Comment on the background quality.
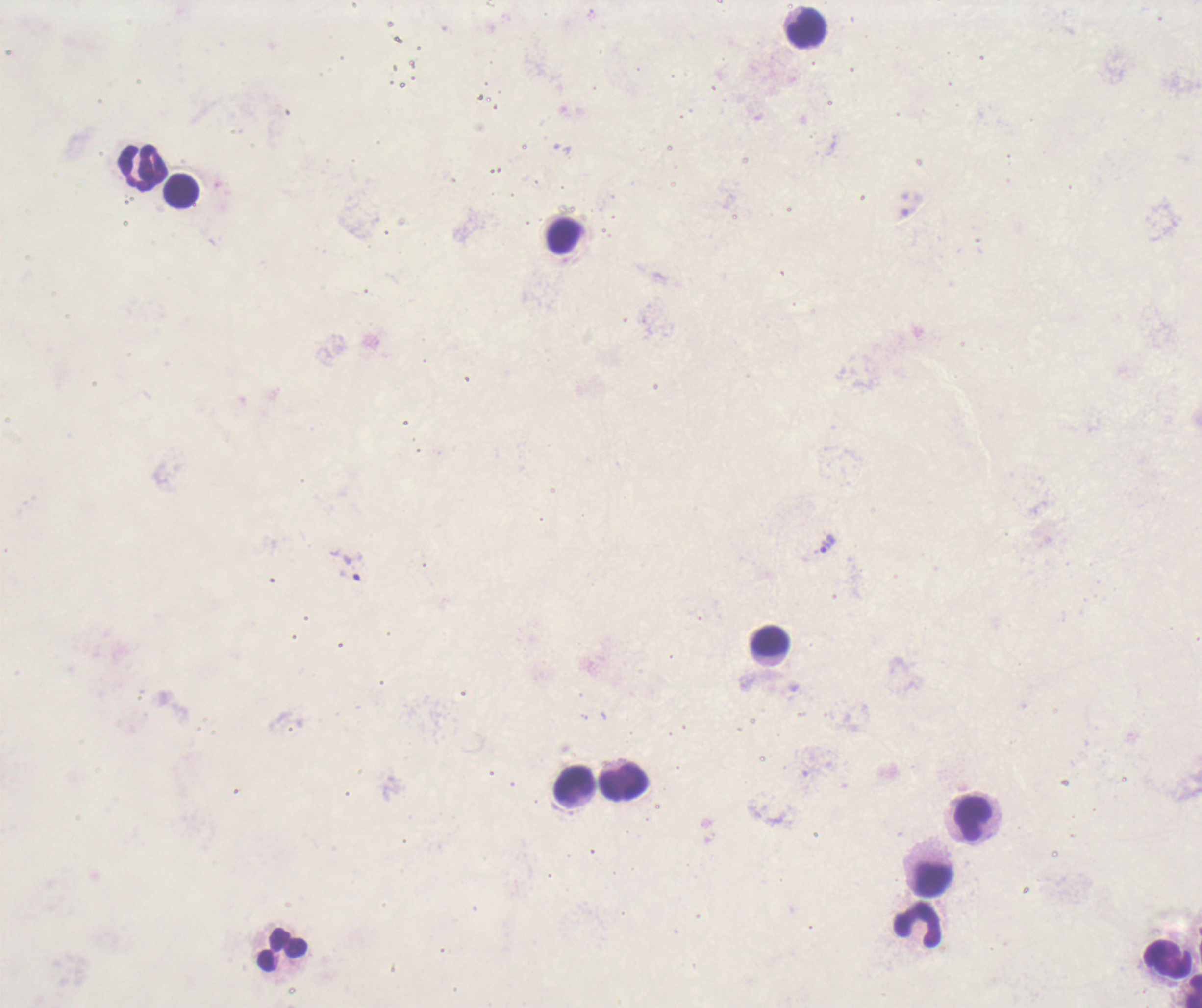

Unsatisfactory.

Approximate centers as (x, y) in pixels. Leukocyte locations: (806, 27), (142, 168), (181, 191), (564, 236), (770, 641), (625, 782), (573, 785), (973, 818), (933, 879), (918, 926), (283, 950), (1168, 960). Trophozoite locations: (825, 546). Thick blood smear. One field from this slide. Coloration quality: bad. Image is 1202×1008 pixels. 100x magnification. Previously used in a real diagnosis. Result: Plasmodium parasites identified. Romanowsky-stained preparation.